Outline each blood parasite and name the species.
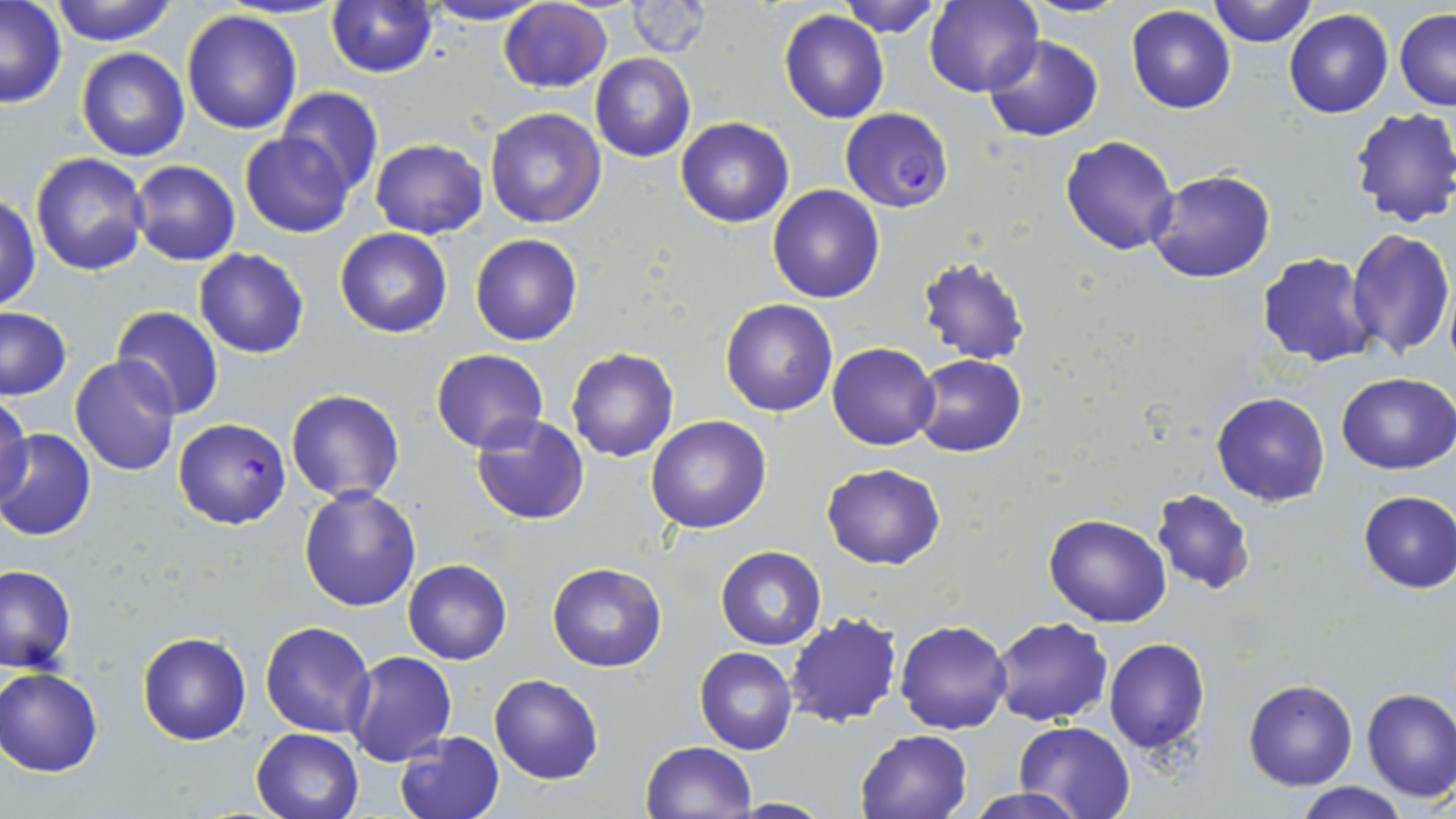
Approximate bounding boxes as (x1,y1)-(x2,y2) corner pairs in pixels.
Plasmodium falciparum-infected red blood cells: (840,107)-(954,212), (174,418)-(291,530).
No Plasmodium ovale, Plasmodium malariae, Plasmodium vivax, Babesia divergens, or Trypanosoma brucei observed.

Uninfected red blood cell locations: (49,0)-(180,47), (325,0)-(438,76), (835,0)-(944,38), (923,0)-(1043,98), (1020,0)-(1136,18), (1205,0)-(1317,48), (417,1)-(551,26), (625,1)-(714,59), (499,2)-(612,93), (0,3)-(68,110), (1125,5)-(1236,115), (182,8)-(303,135), (1284,9)-(1394,118), (1396,9)-(1456,110), (778,10)-(890,124), (983,34)-(1105,142), (76,47)-(190,162), (590,54)-(695,162), (277,87)-(383,196), (483,106)-(606,228), (1350,106)-(1456,228), (675,117)-(794,228), (239,131)-(354,238), (1061,135)-(1179,257), (370,138)-(487,238), (712,144)-(850,273), (30,152)-(151,276), (130,160)-(240,266), (1146,169)-(1276,283), (767,185)-(886,303), (0,194)-(40,313), (335,227)-(453,338), (1346,229)-(1454,359), (469,234)-(584,346), (194,248)-(309,359), (1257,252)-(1381,368), (916,254)-(1032,366), (719,299)-(838,417), (0,307)-(72,400), (110,308)-(225,420), (828,343)-(939,448), (430,348)-(549,454), (567,348)-(679,463), (912,354)-(1026,457), (70,355)-(182,476), (1336,372)-(1456,473), (286,389)-(405,503), (1211,392)-(1331,506), (0,397)-(32,509), (471,414)-(592,525), (646,416)-(771,534), (1,427)-(97,541), (821,463)-(946,568), (297,486)-(421,612), (1151,487)-(1257,596), (1356,489)-(1455,594), (1043,512)-(1171,627), (714,546)-(825,649), (403,558)-(511,665), (547,562)-(667,673), (0,564)-(76,673), (783,612)-(904,729), (987,616)-(1112,727), (895,619)-(1013,735), (260,620)-(377,738), (137,631)-(250,744), (1103,638)-(1209,754), (694,646)-(798,755), (347,652)-(456,766), (0,667)-(104,777), (489,675)-(603,785), (1243,677)-(1358,791), (1361,686)-(1456,801), (355,690)-(482,807), (1013,720)-(1135,819), (251,728)-(364,819), (856,728)-(974,819), (395,730)-(505,819), (641,741)-(758,819), (1293,781)-(1411,819), (962,788)-(1091,819), (725,796)-(829,817). Slide-level diagnosis: Plasmodium falciparum. 1000x magnification. May-Grünwald-Giemsa-stained preparation. Image is 1456×819 pixels. Single field of view. Optical microscopy. Thin blood film.